Classify this cell by malaria status.
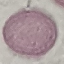
It is uninfected.

Acquired by smartphone through the microscope eyepiece. Giemsa stain. Thin blood film. Automatically extracted cell patch, resized to 64 × 64 pixels.